Name the parasite shown.
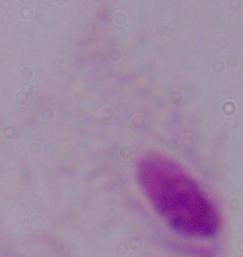

This is a trichomonad.

Micrograph. Captured at 1000x magnification.